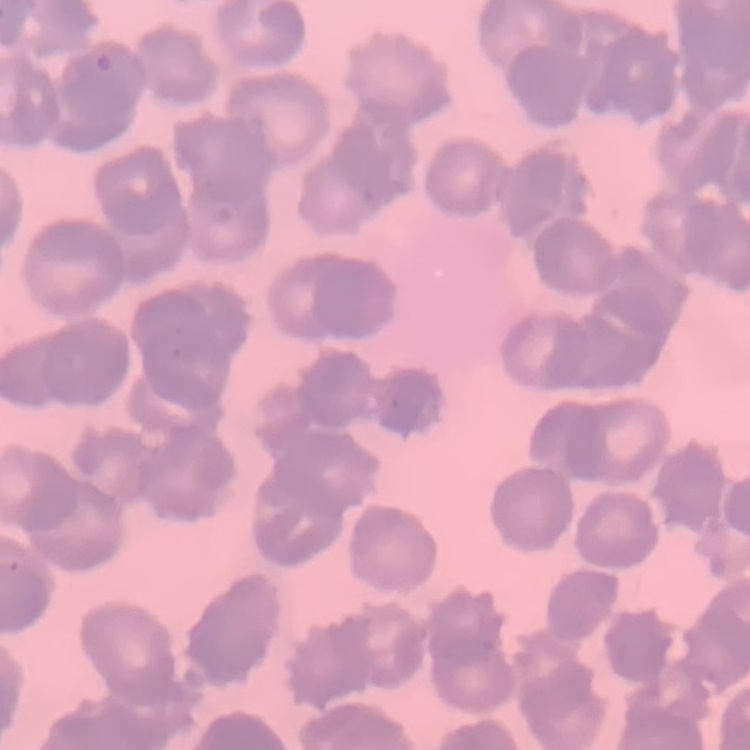
The erythrocytes exhibit rouleaux formation. Square crop of a larger photomicrograph. Stained with either Field's or Giemsa. Thin peripheral smear.